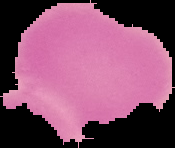
Summary:
  - Preparation: thin blood smear
  - Malaria status: uninfected
  - Image size: 175×148 pixels
  - Image type: segmented cell region with the area outside set to black